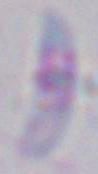

Summary:
  - Magnification: 1000x
  - Identification: Toxoplasma gondii
  - Modality: photomicrograph